Classify this cell by malaria status.
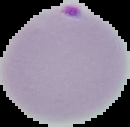
It is parasitized.

Image is 130×127 pixels. From a thin blood smear. Segmented cell region on a black background.